Locate every Plasmodium parasite.
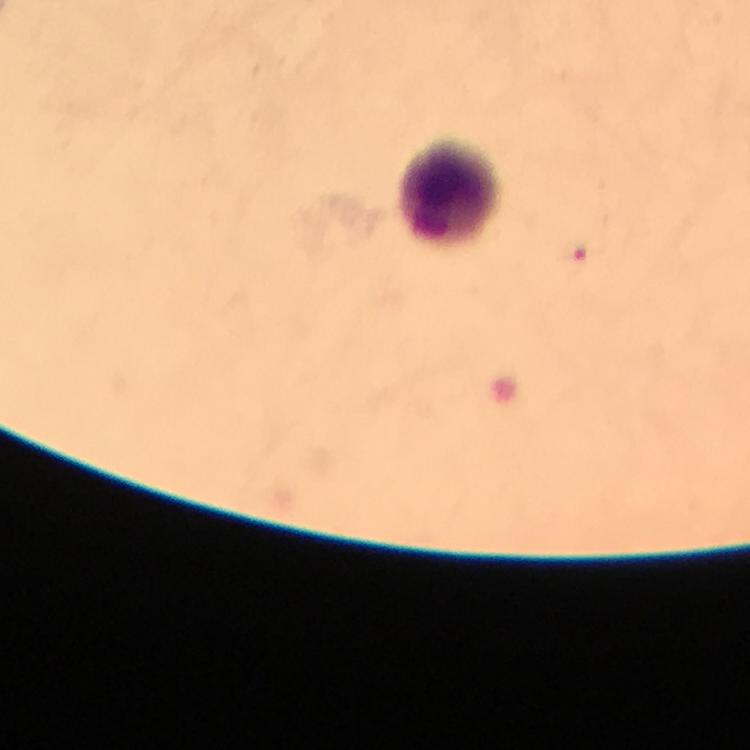
Approximate centers as {x, y} in pixels.
Plasmodium parasites: {575, 255}.

Summary:
  - Leukocyte locations: {452, 194}
  - Image size: 750×750 pixels
  - Magnification: 100x
  - Stain: Giemsa
  - Preparation: thick smear
  - Context: from a diagnostic examination for malaria
  - Capture: smartphone mounted on the microscope
  - Immersion oil: applied
  - Cropped from: one field of view